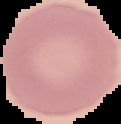

preparation = thin blood film
result = no Plasmodium parasites seen
image size = 121×124 pixels
image type = segmented cell region on a black background